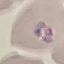
Summary:
  - Malaria status: parasitized
  - Capture: smartphone camera at the microscope eyepiece
  - Image type: cell patch, automatically extracted from a larger field of view and resized to 64 × 64 pixels
  - Preparation: thin blood film
  - Stain: Giemsa